Locate every Plasmodium parasite.
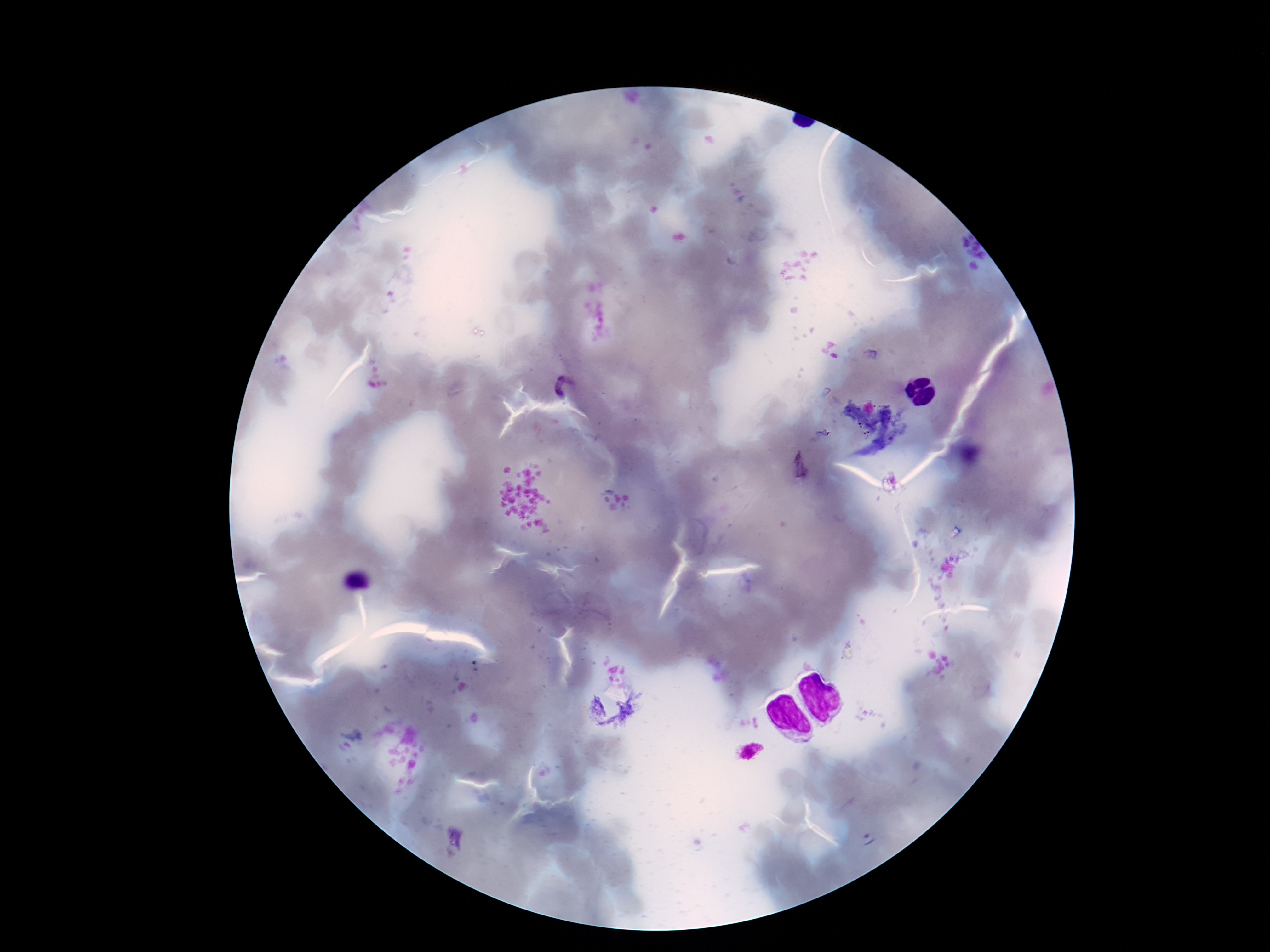
Approximate object centers, in pixels from the top-left corner.
Plasmodium parasites: (x=565, y=388), (x=820, y=436), (x=800, y=466), (x=455, y=840).

Thick peripheral-blood smear. 100x magnification. Giemsa-stained preparation. Patient malaria status: infected. Image is 1270×952 pixels. Smartphone photograph taken through the microscope eyepiece. Single field of view.